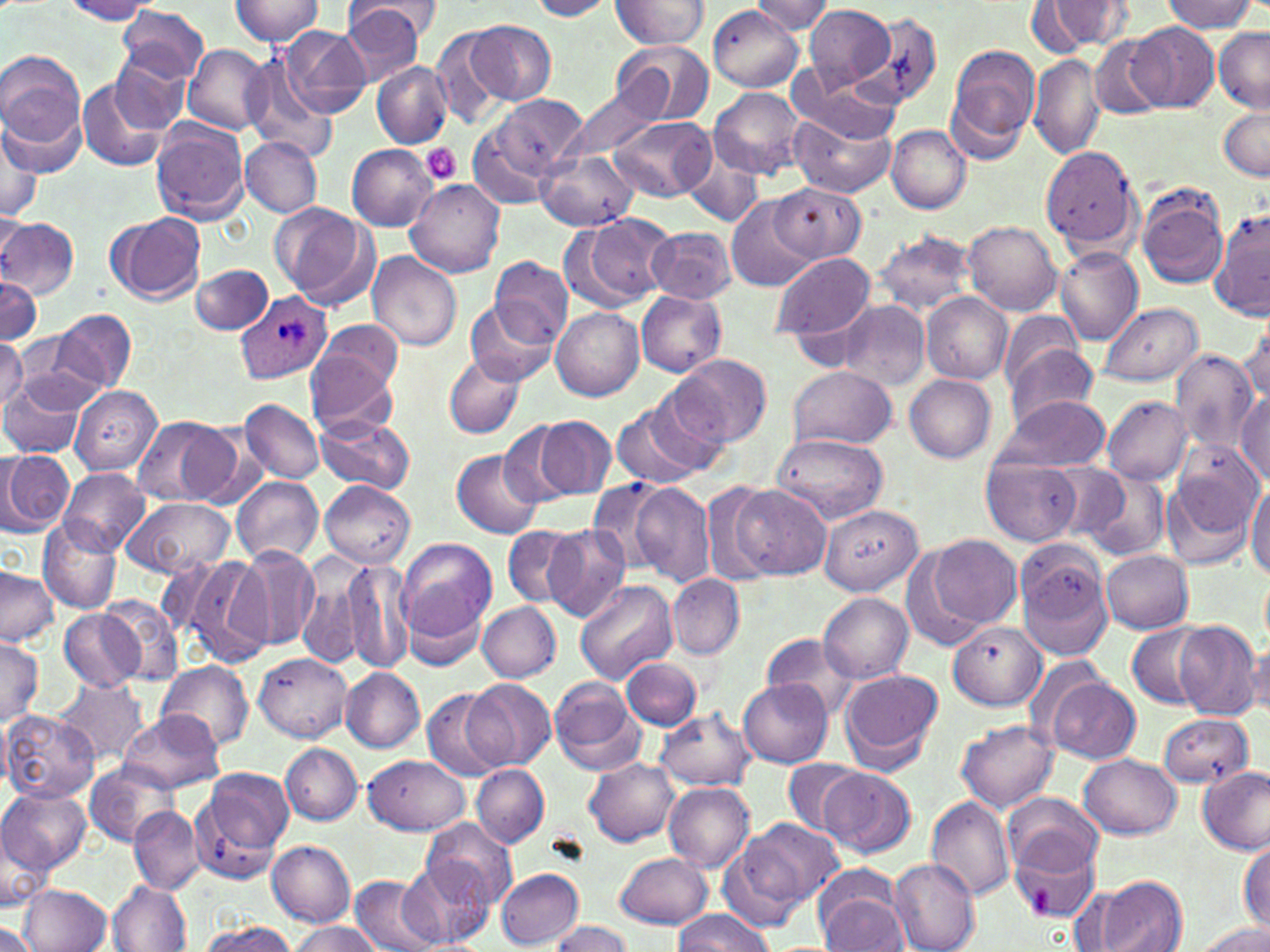
Plasmodium ovale-infected red blood cell locations = approximate bounding boxes as (x1, y1, x2, y2) in pixels: (234, 289, 334, 383)
slide-level diagnosis = Plasmodium ovale
image size = 1270×952 pixels
platelet locations = approximate bounding boxes as (x1, y1, x2, y2) in pixels: (421, 144, 462, 185)
uninfected red blood cell locations = approximate bounding boxes as (x1, y1, x2, y2) in pixels: (232, 0, 324, 45), (527, 0, 614, 21), (610, 0, 710, 49), (1161, 0, 1260, 32), (62, 1, 158, 23), (753, 1, 833, 35), (1036, 1, 1137, 53), (344, 3, 426, 84), (709, 5, 804, 92), (804, 5, 896, 91), (117, 6, 210, 83), (861, 13, 943, 109), (468, 20, 557, 104), (1127, 21, 1219, 112), (278, 25, 371, 119), (431, 26, 507, 128), (1213, 27, 1269, 112), (1088, 33, 1171, 120), (611, 38, 714, 127), (183, 45, 270, 133), (948, 46, 1040, 150), (0, 50, 88, 167), (110, 54, 192, 134), (1029, 54, 1105, 158), (244, 56, 336, 159), (372, 61, 451, 148), (788, 72, 901, 145), (77, 77, 173, 171), (562, 86, 663, 163), (709, 87, 805, 180), (489, 95, 588, 180), (1217, 107, 1270, 181), (790, 111, 896, 197), (609, 116, 714, 202), (151, 121, 252, 224), (0, 123, 41, 225), (886, 125, 972, 213), (468, 129, 553, 210), (242, 137, 322, 218), (346, 145, 436, 232), (1042, 146, 1141, 248), (537, 152, 640, 230), (683, 153, 765, 229), (405, 178, 506, 277), (769, 183, 867, 263), (1135, 184, 1230, 290), (730, 198, 817, 292), (269, 203, 376, 307), (1210, 207, 1270, 321), (105, 212, 207, 304), (573, 214, 676, 309), (0, 217, 79, 298), (965, 220, 1062, 314), (648, 226, 736, 303), (873, 229, 977, 317), (1055, 248, 1144, 344), (368, 251, 463, 352), (772, 252, 877, 344), (490, 258, 573, 348), (191, 264, 274, 335), (0, 275, 41, 348), (636, 291, 726, 377), (920, 292, 1012, 384), (837, 300, 931, 391), (1098, 302, 1204, 386), (467, 303, 556, 384), (552, 307, 644, 401), (50, 310, 136, 393), (1000, 310, 1087, 392), (1239, 312, 1270, 412), (317, 320, 405, 395), (13, 335, 97, 410), (0, 337, 27, 412), (1008, 344, 1099, 424), (1170, 347, 1258, 455), (306, 352, 399, 436), (443, 352, 524, 439), (670, 354, 771, 448), (788, 367, 896, 449), (905, 374, 996, 463), (0, 377, 91, 458), (71, 386, 161, 474), (641, 389, 733, 476), (1236, 391, 1270, 482), (995, 393, 1110, 473), (1101, 396, 1192, 484), (239, 398, 325, 484), (611, 403, 705, 489), (532, 414, 615, 501), (315, 415, 413, 494), (130, 416, 237, 508), (499, 423, 580, 509), (183, 424, 266, 510), (770, 432, 888, 524), (3, 449, 75, 534), (452, 450, 545, 539), (983, 456, 1082, 546), (58, 467, 150, 554), (1079, 470, 1171, 563), (1163, 470, 1260, 571), (233, 477, 324, 563), (585, 478, 671, 574), (320, 481, 414, 567), (629, 481, 716, 586), (1246, 481, 1270, 578), (729, 483, 829, 578), (702, 484, 774, 586), (123, 496, 234, 577), (819, 506, 921, 594), (39, 516, 125, 613), (502, 525, 582, 608), (543, 526, 632, 623), (395, 536, 498, 647), (929, 536, 1021, 629), (1014, 539, 1113, 656), (238, 546, 321, 651), (902, 548, 988, 652), (1102, 550, 1194, 634), (181, 554, 274, 669), (295, 555, 375, 673), (342, 559, 415, 674), (0, 569, 58, 647), (668, 573, 744, 658), (576, 578, 677, 683), (819, 591, 915, 683), (101, 598, 183, 687), (477, 601, 561, 681), (58, 606, 145, 692), (1172, 621, 1263, 719), (949, 622, 1047, 710), (1127, 624, 1209, 709), (759, 632, 860, 716), (0, 635, 44, 728), (1244, 640, 1270, 719), (252, 654, 351, 741), (622, 658, 702, 729), (156, 660, 254, 750), (838, 667, 942, 769), (341, 668, 425, 752), (549, 675, 642, 773), (1044, 677, 1140, 764), (467, 678, 556, 768), (56, 679, 147, 766), (738, 680, 833, 767), (420, 686, 509, 782), (656, 708, 755, 791), (0, 711, 99, 803), (119, 711, 224, 793), (1159, 712, 1254, 788), (957, 719, 1059, 812), (281, 743, 363, 825), (1080, 754, 1181, 839), (363, 756, 470, 835), (585, 757, 680, 847), (782, 759, 863, 836), (82, 761, 177, 848), (472, 764, 549, 847), (197, 766, 295, 870), (818, 766, 915, 859), (1199, 767, 1269, 853), (663, 781, 755, 872), (0, 786, 91, 875), (1003, 790, 1105, 878), (925, 797, 1015, 902), (128, 804, 204, 894), (422, 818, 518, 912), (735, 818, 844, 912), (0, 830, 51, 910), (1009, 837, 1103, 923), (1238, 839, 1269, 935), (267, 841, 355, 926), (615, 852, 714, 929), (888, 859, 980, 952), (402, 861, 494, 945), (496, 868, 585, 948), (350, 874, 447, 952), (1091, 876, 1187, 952), (108, 883, 191, 952), (19, 884, 112, 952), (818, 888, 910, 951), (675, 909, 773, 951), (289, 920, 382, 952), (551, 921, 634, 952), (1193, 921, 1269, 952), (0, 922, 43, 952), (197, 922, 298, 952)
modality = light microscopy
magnification = 1000x
stain = May-Grünwald-Giemsa
field of view = single
preparation = thin blood film